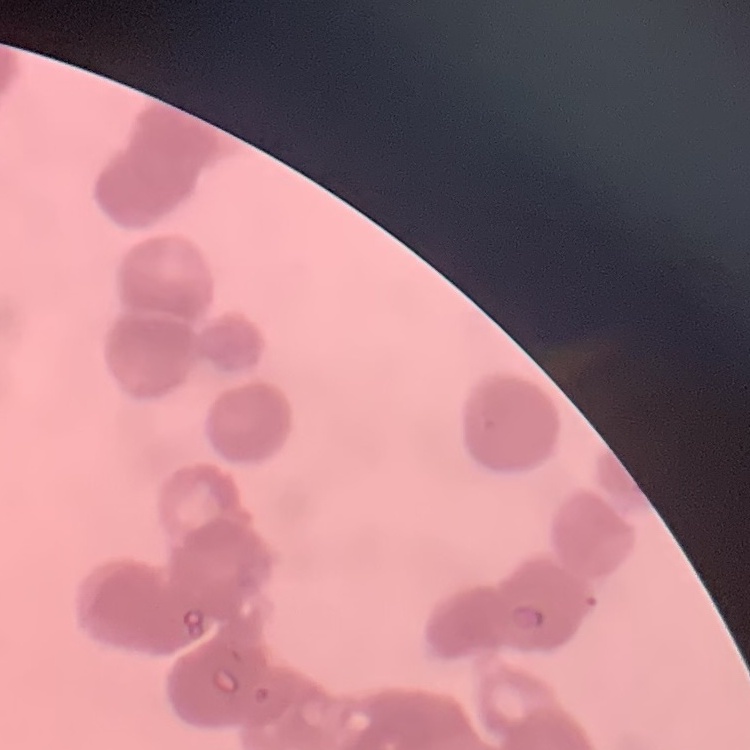
Summary:
  - Erythrocyte morphology: rouleaux formation
  - Preparation: thin peripheral smear
  - Image type: square crop of a larger photomicrograph
  - Stain: Field's or Giemsa